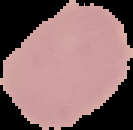
Image is 133×130 pixels. Result: no malaria parasites detected. Segmented cell region on a black background. From a thin blood smear.